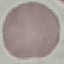
malaria status = uninfected
stain = Giemsa
capture = smartphone through the microscope eyepiece
image type = cell patch, automatically extracted from a larger field of view and resized to 64 × 64 pixels
preparation = thin blood smear